Classify this cell by malaria status.
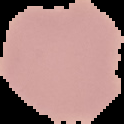
Uninfected.

From a thin blood smear. The area outside the segmented cell region is set to black. Image is 124×124 pixels.